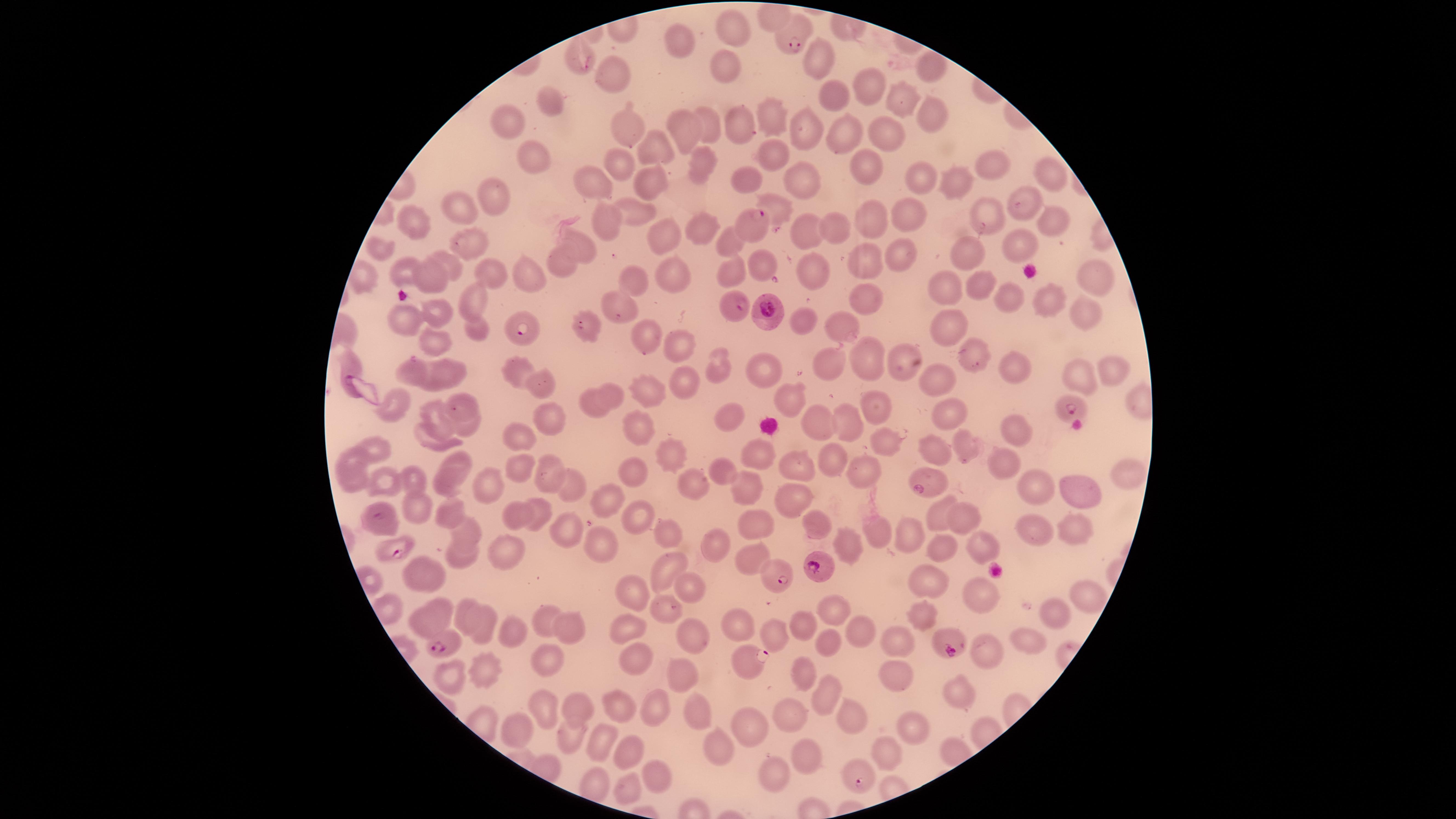
image size = 1456×819 pixels
uninfected RBCs = approximate marker points as (x, y) in pixels: (774, 18), (730, 27), (680, 42), (578, 52), (818, 58), (723, 67), (617, 71), (925, 72), (867, 86), (833, 100), (901, 100), (553, 106), (930, 114), (770, 117), (625, 123), (739, 124), (510, 125), (714, 128), (690, 130), (807, 131), (843, 136), (888, 139), (661, 154), (771, 154), (699, 159), (525, 161), (620, 162), (867, 165), (997, 165), (1054, 175), (747, 179), (918, 181), (593, 182), (646, 182), (803, 184), (951, 189), (497, 198), (774, 204), (1020, 205), (461, 208), (636, 208), (909, 217), (871, 218), (990, 218), (417, 219), (1049, 222), (607, 224), (698, 228), (803, 230), (836, 230), (661, 232), (727, 238), (469, 240), (577, 242), (1024, 242), (960, 243), (381, 250), (901, 250), (562, 258), (863, 260), (757, 263), (452, 265), (731, 271), (488, 272), (410, 273), (815, 273), (431, 274), (671, 275), (361, 277), (530, 278), (1093, 281), (631, 286), (980, 288), (946, 289), (1008, 297), (867, 299), (1045, 299), (472, 302), (439, 308), (614, 310), (1085, 316), (407, 321), (803, 321), (842, 325), (941, 327), (481, 331), (647, 341), (430, 342), (674, 343), (971, 357), (867, 358), (902, 361), (767, 363), (721, 364), (350, 365), (824, 366), (1007, 367), (451, 369), (1117, 369), (516, 371), (412, 372), (1071, 373), (683, 385), (546, 386), (652, 386), (937, 386), (611, 390), (787, 397), (592, 398), (394, 402), (466, 402), (877, 404), (945, 413), (547, 417), (734, 420), (848, 421), (815, 422), (445, 427), (471, 427), (644, 428), (1010, 428), (426, 436), (522, 436), (883, 441), (375, 448), (936, 449), (964, 449), (756, 454), (351, 457), (669, 457), (456, 460), (830, 461), (1001, 464), (547, 466), (519, 468), (798, 470), (860, 473), (638, 475), (719, 475), (414, 476), (1121, 476), (385, 481), (348, 483), (690, 484), (488, 486), (568, 487), (750, 487), (1035, 488), (443, 491), (1072, 493), (790, 499), (607, 501), (415, 508), (448, 510), (544, 511), (517, 512), (963, 514), (633, 517), (938, 517), (750, 523), (1073, 524), (812, 525), (875, 525), (466, 532), (566, 532), (667, 532), (1027, 533), (900, 535), (601, 544), (849, 544), (984, 544), (715, 546), (506, 547), (939, 552), (750, 556), (460, 561), (666, 567), (429, 570), (930, 582), (690, 585), (981, 589), (631, 591), (1086, 595), (440, 606), (663, 607), (828, 607), (473, 610), (1055, 612), (924, 619), (547, 621), (797, 621), (571, 625), (420, 626), (485, 628), (625, 628), (740, 629), (857, 630), (774, 631), (512, 635), (691, 637), (897, 639), (827, 641), (1025, 641), (985, 651), (633, 658), (545, 665), (483, 670), (804, 672), (679, 673), (894, 675), (452, 676), (822, 693), (963, 699), (577, 706), (617, 708), (697, 709), (653, 710), (549, 711), (847, 715), (788, 718), (912, 727), (750, 729), (521, 731), (572, 735), (601, 740), (718, 744), (626, 755), (808, 755), (889, 755), (661, 771), (770, 774), (631, 787)
species = Plasmodium falciparum
parasitized RBCs = approximate marker points as (x, y) in pixels: (793, 39), (758, 225), (735, 304), (769, 310), (581, 327), (519, 331), (1074, 408), (922, 485), (379, 517), (399, 557), (817, 565), (775, 577), (948, 646), (441, 649), (746, 659), (860, 777)
visible region = circular
field of view = single
stain = Giemsa
preparation = thin blood film
presence = malaria parasites identified
capture = smartphone photograph through the microscope eyepiece